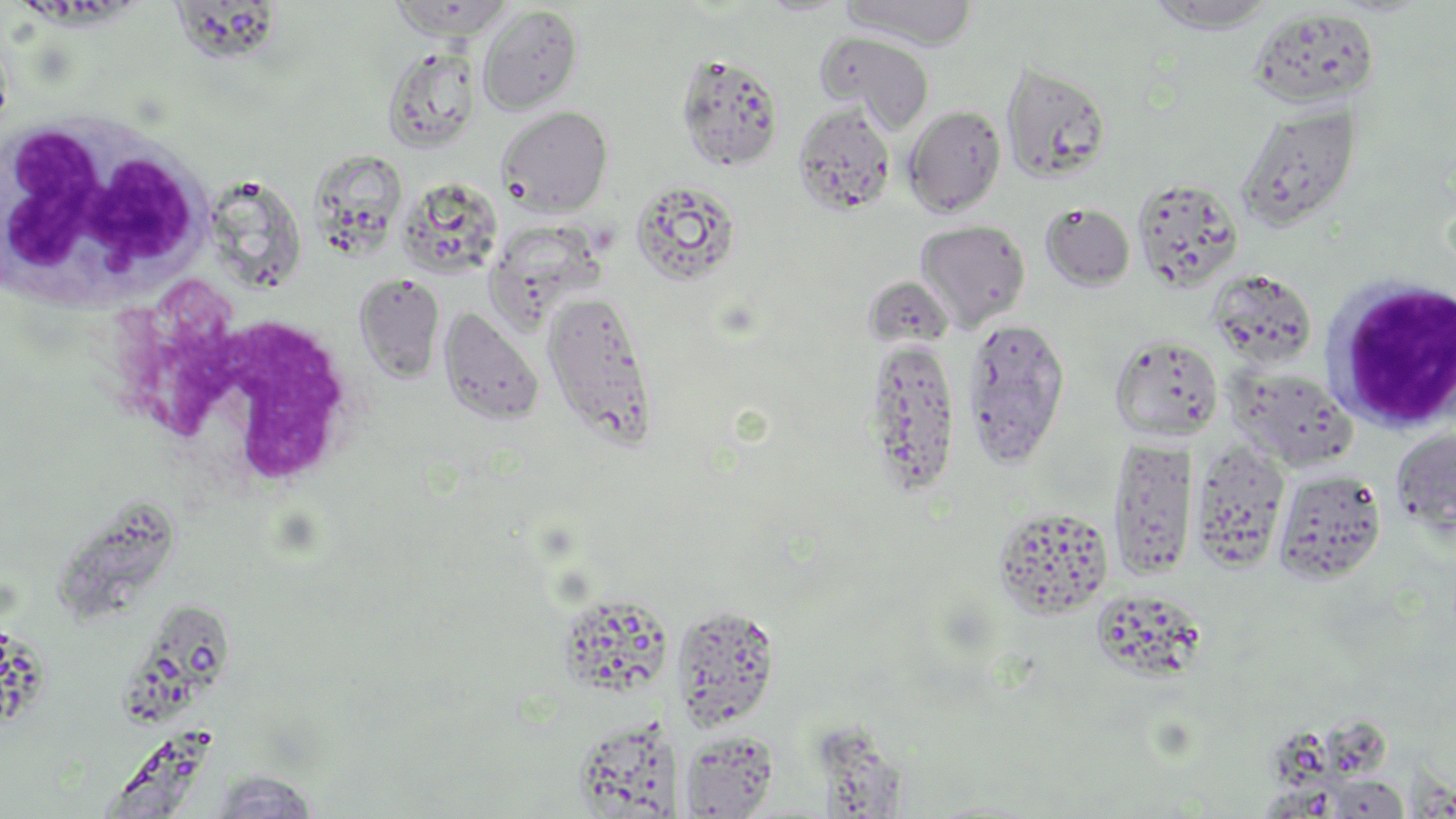
Approximate bounding boxes as [x1, y1, x2, y2] in pixels. Uninfected red blood cell locations: [390, 0, 515, 40], [842, 0, 977, 48], [1145, 1, 1278, 33], [478, 4, 583, 115], [169, 5, 279, 64], [1248, 7, 1379, 109], [818, 31, 934, 132], [382, 45, 482, 154], [676, 53, 785, 172], [1001, 61, 1112, 182], [792, 104, 896, 217], [1234, 104, 1361, 231], [903, 105, 1007, 217], [496, 106, 613, 215], [318, 148, 410, 266], [216, 168, 308, 297], [1131, 176, 1244, 291], [401, 179, 507, 277], [629, 179, 743, 286], [1041, 203, 1134, 291], [915, 220, 1031, 331], [487, 225, 613, 328], [1206, 268, 1319, 369], [354, 273, 445, 383], [865, 274, 949, 337], [542, 290, 658, 446], [439, 307, 544, 426], [960, 317, 1071, 467], [1109, 334, 1224, 442], [864, 337, 961, 498], [1227, 366, 1357, 471], [1390, 426, 1456, 540], [1108, 437, 1198, 579], [1190, 440, 1290, 573], [1272, 468, 1387, 585], [56, 495, 182, 620], [991, 505, 1113, 619], [1095, 596, 1209, 682], [559, 599, 668, 691], [118, 600, 227, 729], [671, 604, 781, 731], [1, 619, 51, 726], [812, 719, 906, 818], [579, 721, 686, 817], [109, 729, 217, 818], [680, 729, 778, 818], [201, 770, 327, 817], [1320, 774, 1413, 817]. White blood cell locations: [1, 112, 212, 315], [1322, 276, 1456, 434], [126, 306, 368, 501]. Slide-level diagnosis: no evidence of blood parasites. May-Grünwald-Giemsa stain. Single field of view. Light microscopy. Captured at 1000x magnification. Image is 1456×819 pixels. Thin blood film.